Assess the morphology of the red blood cells.
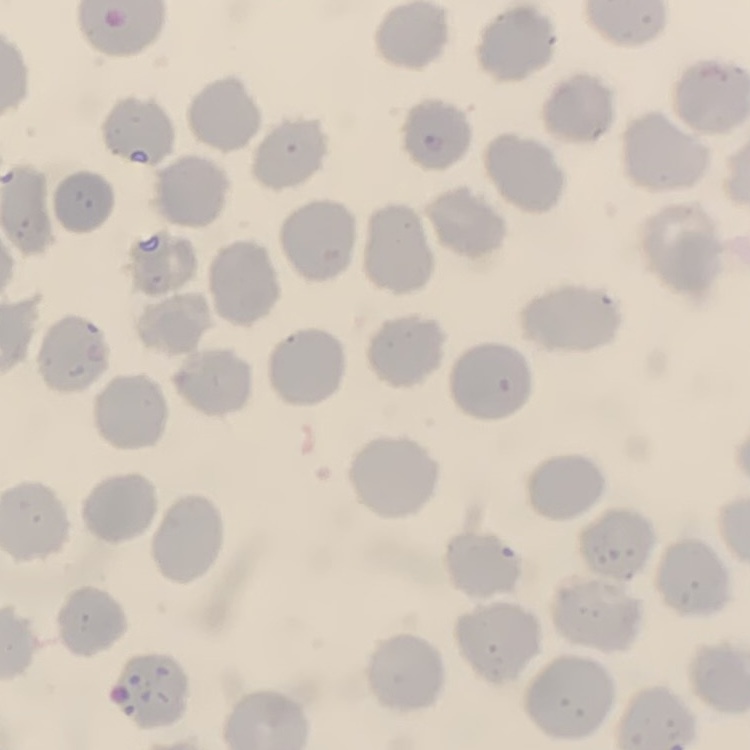

No rouleaux formation.

Field's or Giemsa stain. Thin peripheral smear. One tile cut from a larger photomicrograph.